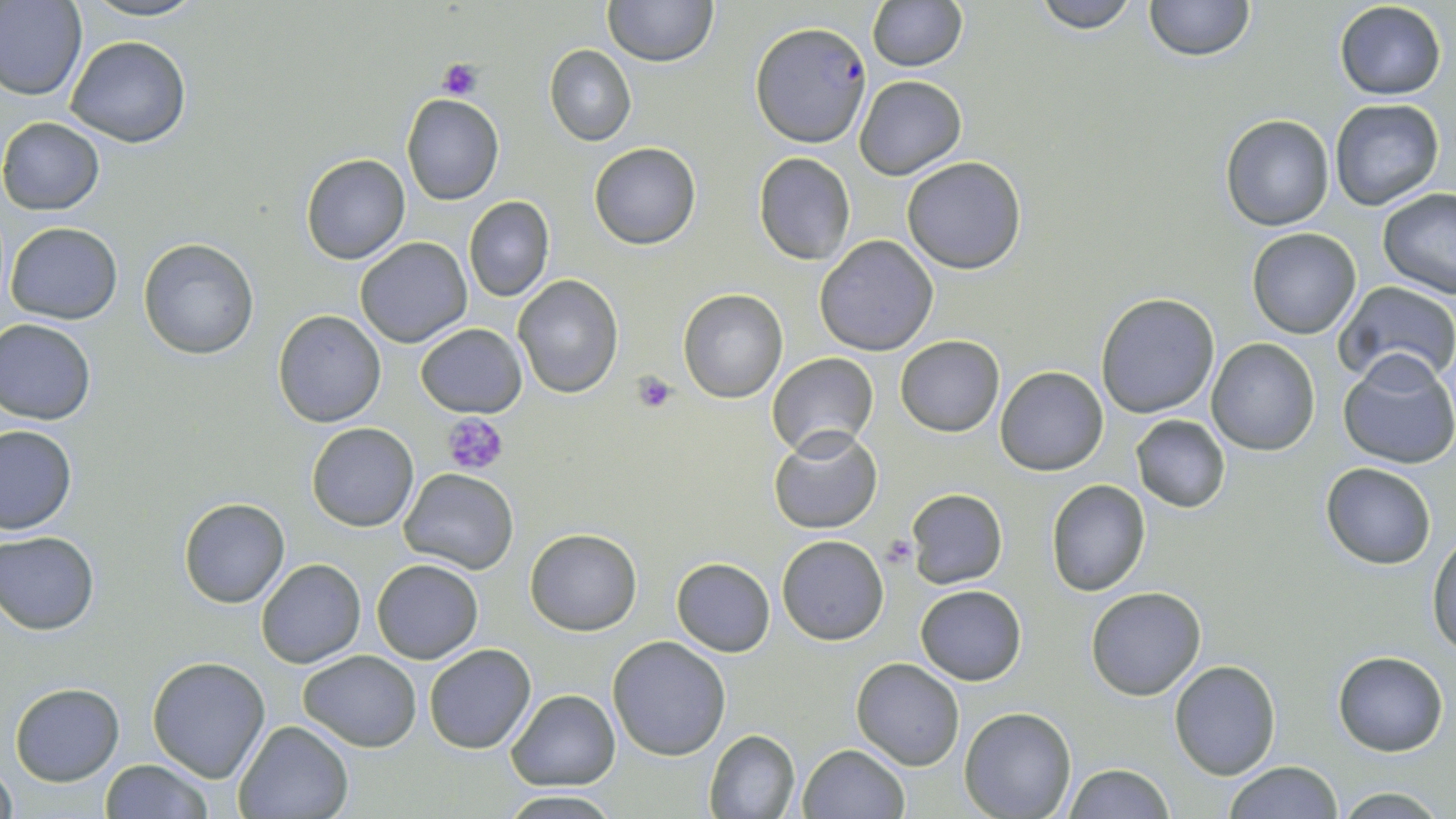 Approximate bounding boxes as (x1, y1, x2, y2) in pixels. Platelet locations: (439, 58, 481, 100), (630, 371, 678, 414), (443, 412, 509, 476), (882, 535, 915, 566). Plasmodium falciparum-infected red blood cell locations: (753, 22, 875, 150). Uninfected red blood cell locations: (0, 0, 87, 103), (78, 0, 207, 23), (604, 0, 717, 67), (1030, 0, 1145, 32), (1143, 0, 1254, 61), (867, 1, 967, 72), (1334, 1, 1447, 101), (65, 36, 192, 148), (545, 45, 636, 145), (855, 74, 966, 182), (401, 95, 503, 205), (1328, 98, 1444, 210), (1220, 114, 1335, 231), (1, 117, 104, 215), (590, 143, 701, 250), (753, 152, 858, 266), (300, 153, 411, 264), (902, 157, 1028, 274), (1378, 187, 1456, 298), (463, 195, 554, 303), (4, 221, 124, 324), (1247, 228, 1362, 339), (814, 235, 939, 356), (355, 237, 471, 347), (138, 239, 258, 358), (513, 275, 624, 398), (1333, 281, 1456, 388), (678, 288, 786, 402), (1095, 291, 1220, 418), (273, 311, 387, 428), (0, 319, 97, 424), (415, 322, 526, 417), (896, 335, 1004, 437), (1208, 338, 1321, 455), (1338, 351, 1456, 469), (767, 352, 880, 459), (994, 366, 1108, 477), (1131, 415, 1231, 513), (306, 423, 418, 532), (0, 424, 76, 534), (769, 428, 883, 534), (1320, 462, 1435, 568), (399, 468, 517, 574), (1045, 480, 1151, 597), (904, 489, 1008, 587), (178, 498, 290, 608), (525, 529, 641, 635), (1, 530, 99, 634), (776, 534, 889, 644), (1429, 535, 1456, 660), (672, 557, 776, 656), (256, 558, 365, 668), (372, 558, 484, 663), (915, 584, 1026, 685), (1084, 585, 1208, 700), (608, 637, 730, 759), (424, 644, 537, 753), (297, 650, 421, 749), (1334, 651, 1448, 756), (148, 656, 271, 782), (850, 658, 964, 770), (1169, 660, 1282, 780), (10, 681, 124, 785), (507, 689, 620, 790), (959, 708, 1075, 819), (235, 718, 354, 819), (703, 729, 801, 818), (797, 744, 908, 819), (99, 758, 214, 818), (1223, 760, 1344, 818), (1, 763, 16, 819), (1062, 764, 1174, 819), (1332, 786, 1450, 818), (497, 791, 624, 818). Slide-level diagnosis: Plasmodium falciparum. 1000x magnification. Thin blood film. Single field of view. May-Grünwald-Giemsa stain. Light microscopy. Image is 1456×819 pixels.